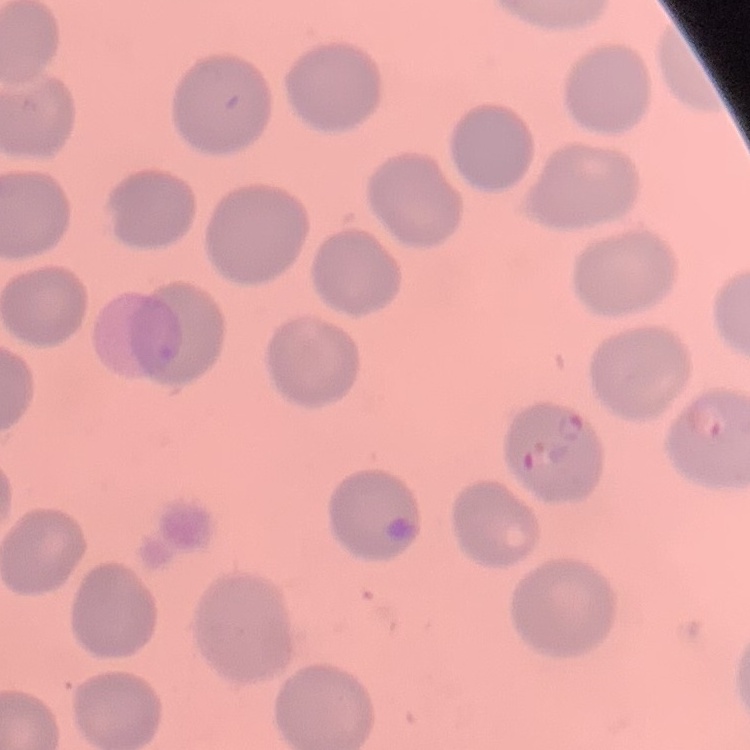 The red blood cells exhibit no rouleaux formation. One tile cut from a larger photomicrograph. Thin blood film. Stained with either Field's or Giemsa.